Assess the morphology of the red blood cells.
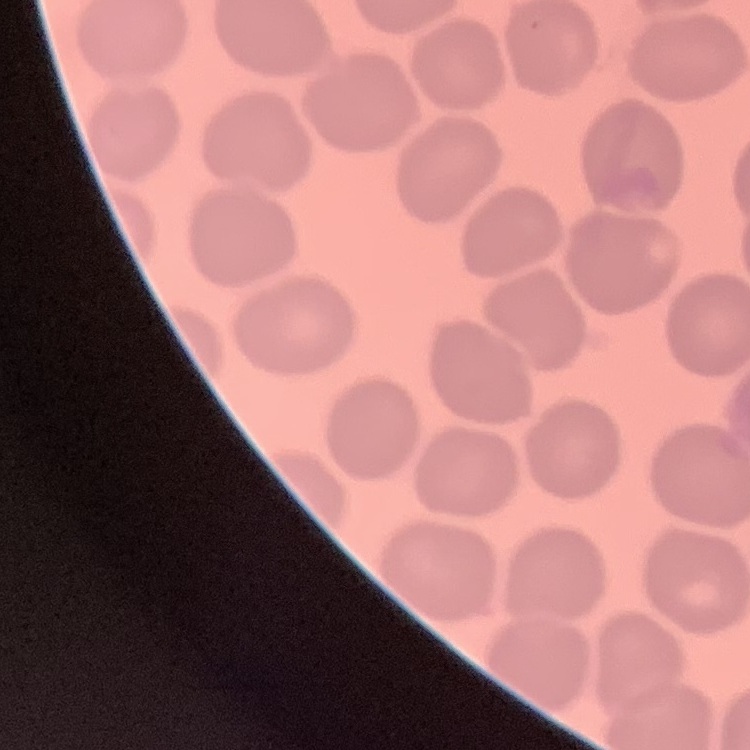

No rouleaux formation.

stain: Field's or Giemsa
preparation: thin peripheral smear
image_type: square crop of a larger photomicrograph